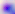

Photomicrograph. Toxoplasma gondii is seen. 400x magnification.